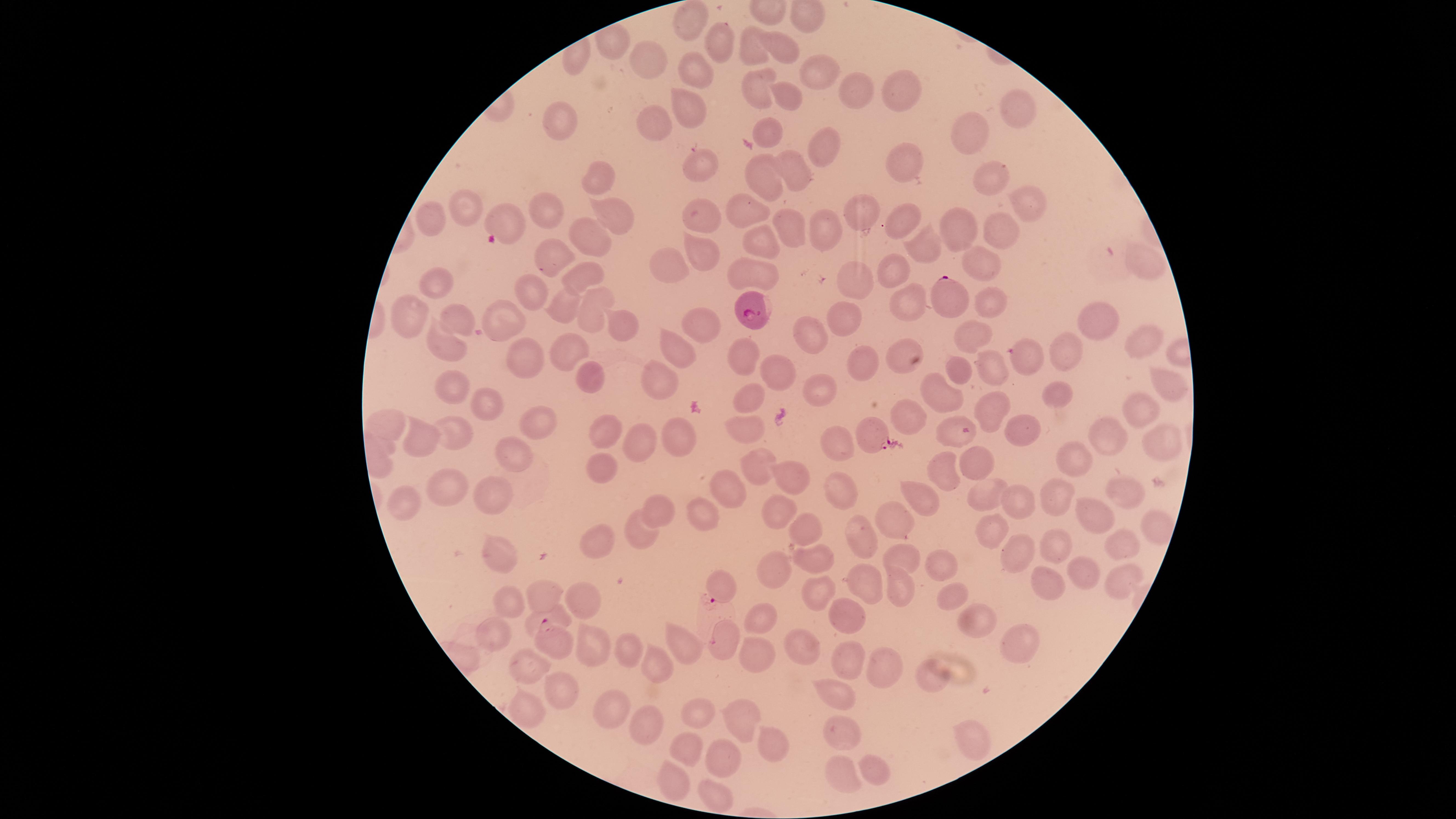
{
  "uninfected_red_blood_cells": "approximate marker points as {x, y} in pixels: {688, 23}, {717, 44}, {783, 49}, {753, 52}, {652, 57}, {694, 72}, {821, 74}, {752, 90}, {900, 93}, {863, 95}, {785, 96}, {690, 108}, {1016, 110}, {656, 120}, {561, 125}, {769, 129}, {968, 134}, {823, 143}, {697, 160}, {900, 164}, {790, 169}, {985, 171}, {766, 175}, {602, 177}, {1026, 189}, {753, 208}, {542, 210}, {457, 211}, {617, 212}, {860, 212}, {706, 215}, {508, 220}, {435, 221}, {905, 222}, {831, 223}, {791, 226}, {961, 229}, {999, 229}, {761, 235}, {594, 240}, {926, 243}, {701, 248}, {548, 249}, {977, 260}, {663, 261}, {761, 269}, {1140, 269}, {894, 275}, {584, 276}, {856, 278}, {444, 279}, {530, 293}, {903, 299}, {562, 300}, {990, 302}, {590, 303}, {408, 310}, {454, 319}, {844, 322}, {506, 323}, {701, 323}, {1094, 323}, {617, 328}, {815, 329}, {970, 333}, {1145, 339}, {682, 342}, {569, 344}, {444, 347}, {898, 352}, {1064, 354}, {524, 355}, {744, 356}, {1027, 360}, {864, 362}, {995, 367}, {956, 368}, {777, 369}, {664, 374}, {590, 375}, {1169, 384}, {819, 388}, {447, 390}, {1056, 390}, {750, 394}, {942, 398}, {490, 399}, {1132, 406}, {986, 409}, {902, 415}, {748, 419}, {540, 424}, {1016, 424}, {393, 425}, {944, 430}, {604, 431}, {677, 431}, {1161, 431}, {1102, 435}, {643, 437}, {452, 440}, {837, 443}, {426, 444}, {511, 452}, {980, 452}, {1078, 455}, {602, 466}, {764, 466}, {946, 471}, {793, 479}, {731, 485}, {927, 488}, {493, 490}, {1123, 490}, {444, 491}, {989, 494}, {833, 495}, {406, 497}, {1023, 501}, {1055, 502}, {775, 508}, {657, 510}, {704, 514}, {1094, 514}, {898, 518}, {1145, 525}, {798, 533}, {991, 533}, {637, 536}, {602, 539}, {855, 539}, {1119, 541}, {1055, 545}, {497, 554}, {1008, 555}, {904, 556}, {816, 557}, {946, 561}, {775, 567}, {1077, 569}, {1113, 578}, {1048, 581}, {871, 584}, {720, 586}, {897, 588}, {548, 593}, {584, 596}, {953, 596}, {816, 598}, {505, 606}, {556, 614}, {849, 616}, {974, 617}, {761, 619}, {494, 635}, {722, 641}, {1011, 641}, {797, 643}, {592, 647}, {681, 649}, {629, 651}, {758, 653}, {848, 657}, {529, 663}, {656, 665}, {879, 670}, {932, 673}, {557, 688}, {843, 693}, {611, 705}, {525, 707}, {700, 711}, {736, 717}, {647, 726}, {837, 729}, {974, 737}, {687, 745}, {769, 745}, {720, 763}, {871, 770}, {843, 773}, {673, 779}, {710, 798}",
  "capture": "smartphone photograph through the microscope eyepiece",
  "image_size": "1456×819 pixels",
  "presence": "malaria parasites seen",
  "preparation": "thin blood film",
  "parasitized_red_blood_cells": "approximate marker points as {x, y} in pixels: {946, 298}, {754, 307}, {875, 434}, {710, 614}, {549, 641}",
  "visible_region": "circular",
  "field_of_view": "single",
  "stain": "Giemsa",
  "species": "Plasmodium falciparum"
}